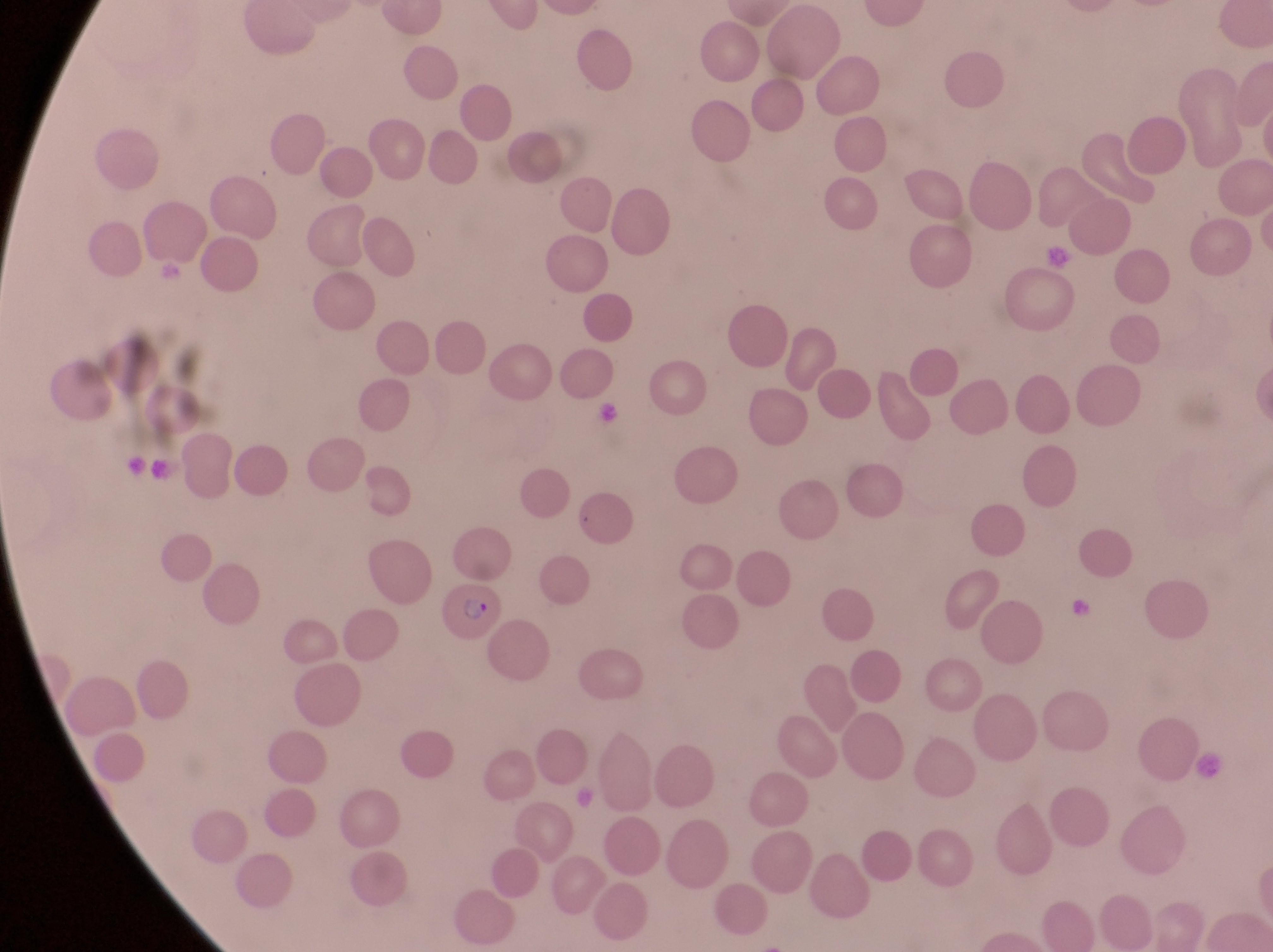 Approximate bounding boxes as {left, top, right, bottom} in pixels. Artifact (platelet-like body, stain precipitate, or debris) locations: {1041, 240, 1078, 273}, {594, 397, 631, 434}, {1071, 592, 1101, 625}, {1193, 754, 1230, 789}. Parasitised red blood cell locations: {440, 584, 507, 647}. Thin blood smear. Image is 1273×952 pixels. Captured by a smartphone held over the eyepiece of an Olympus CX-23 microscope. One field of view. Sample from Uganda. Magnification of 1000x.